Classify this cell by malaria status.
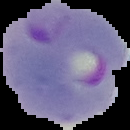
Parasitized.

Summary:
  - Image type: cell region segmented out of the field of view; surrounding area masked to black
  - Preparation: thin blood film
  - Image size: 130×130 pixels